Describe the morphology of the erythrocytes.
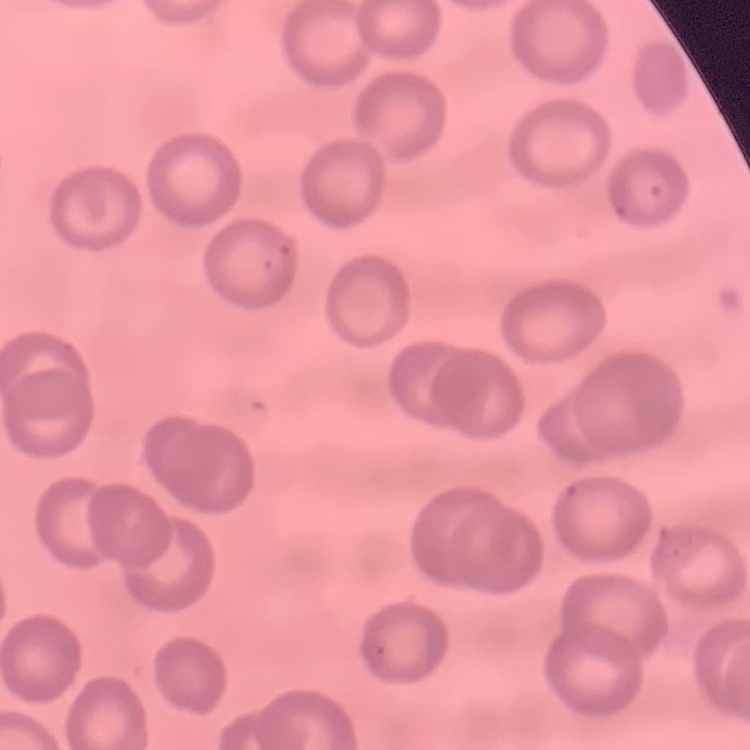

They show no rouleaux formation.

Thin blood smear. Square crop of a larger photomicrograph. Field's or Giemsa stain.